Name the parasite shown.
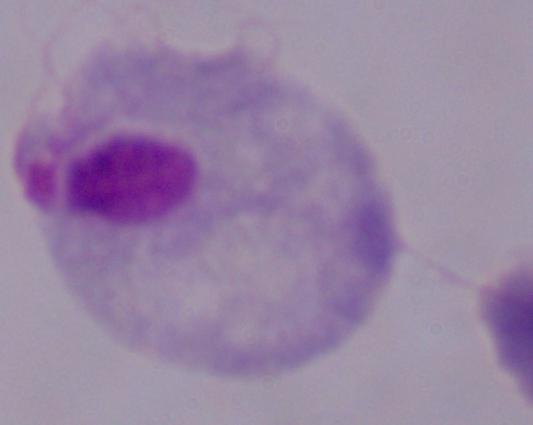

This is a trichomonad.

modality = micrograph
magnification = 1000x